Outline each uninfected red blood cell.
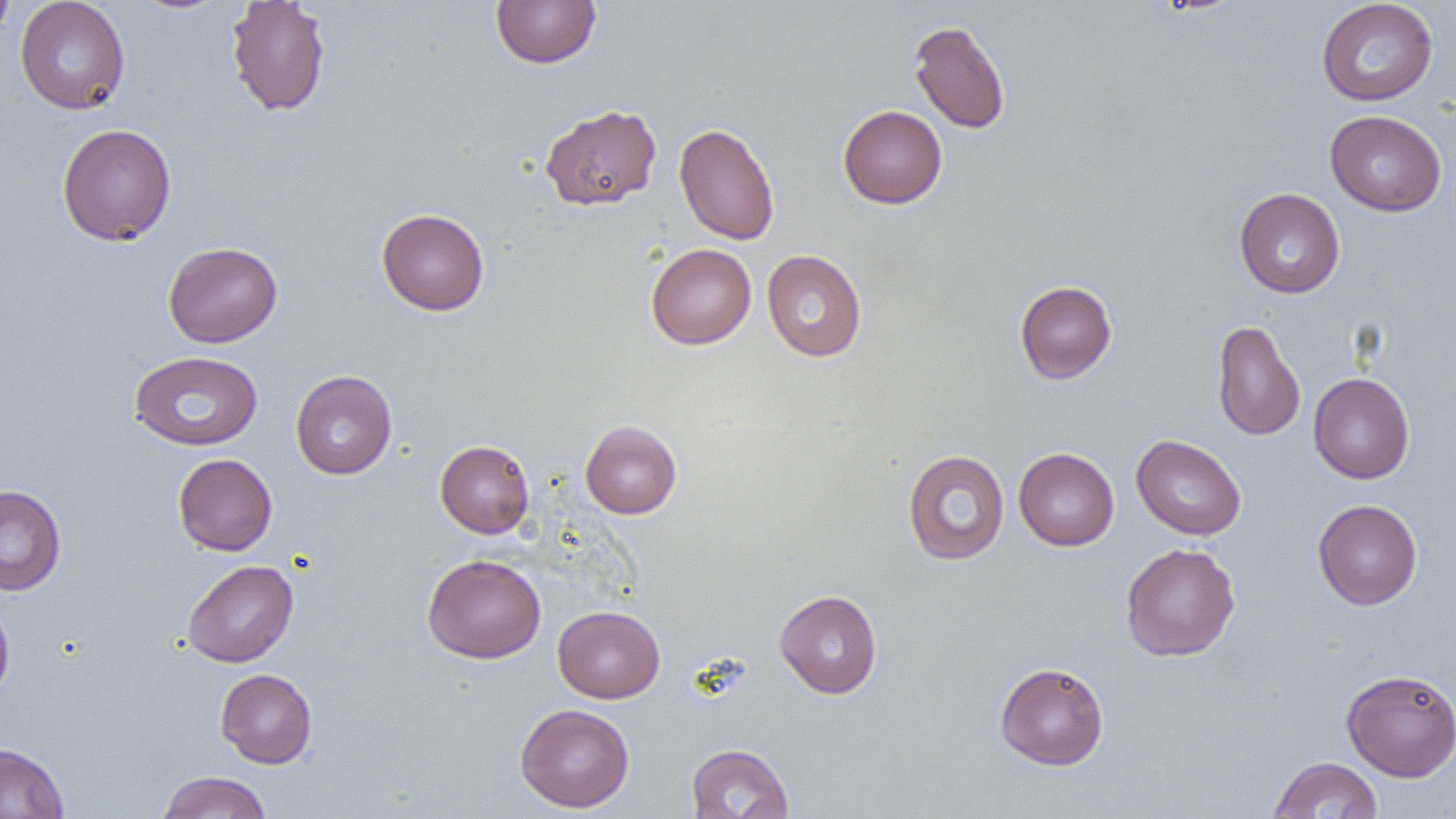
Approximate bounding boxes as [x1, y1, x2, y2] in pixels.
Uninfected red blood cells: [0, 0, 16, 42], [14, 0, 130, 115], [225, 0, 332, 117], [491, 0, 601, 68], [1316, 0, 1439, 106], [908, 19, 1011, 134], [540, 104, 662, 210], [838, 105, 947, 209], [1325, 110, 1447, 216], [674, 122, 780, 245], [57, 123, 176, 246], [1234, 187, 1345, 298], [376, 208, 489, 315], [163, 241, 283, 347], [646, 243, 756, 349], [762, 249, 867, 362], [1014, 280, 1117, 383], [1211, 319, 1305, 441], [129, 350, 264, 451], [291, 369, 397, 479], [1308, 372, 1415, 484], [580, 420, 682, 519], [1131, 434, 1246, 540], [435, 439, 535, 539], [1013, 448, 1119, 551], [902, 449, 1010, 565], [173, 453, 277, 556], [0, 484, 66, 595], [1313, 499, 1423, 610], [1120, 543, 1240, 661], [422, 554, 546, 663], [182, 560, 299, 668], [774, 589, 883, 698], [0, 596, 15, 704], [553, 605, 665, 703], [994, 661, 1109, 770], [215, 668, 318, 768], [1341, 668, 1456, 781], [514, 704, 635, 812], [0, 743, 69, 819], [686, 743, 794, 819], [1268, 756, 1383, 819], [156, 771, 272, 818].

Slide-level diagnosis: negative for blood parasites. Thin blood smear. Single field of view. Optical microscopy. Captured at 1000x magnification. Image is 1456×819 pixels.